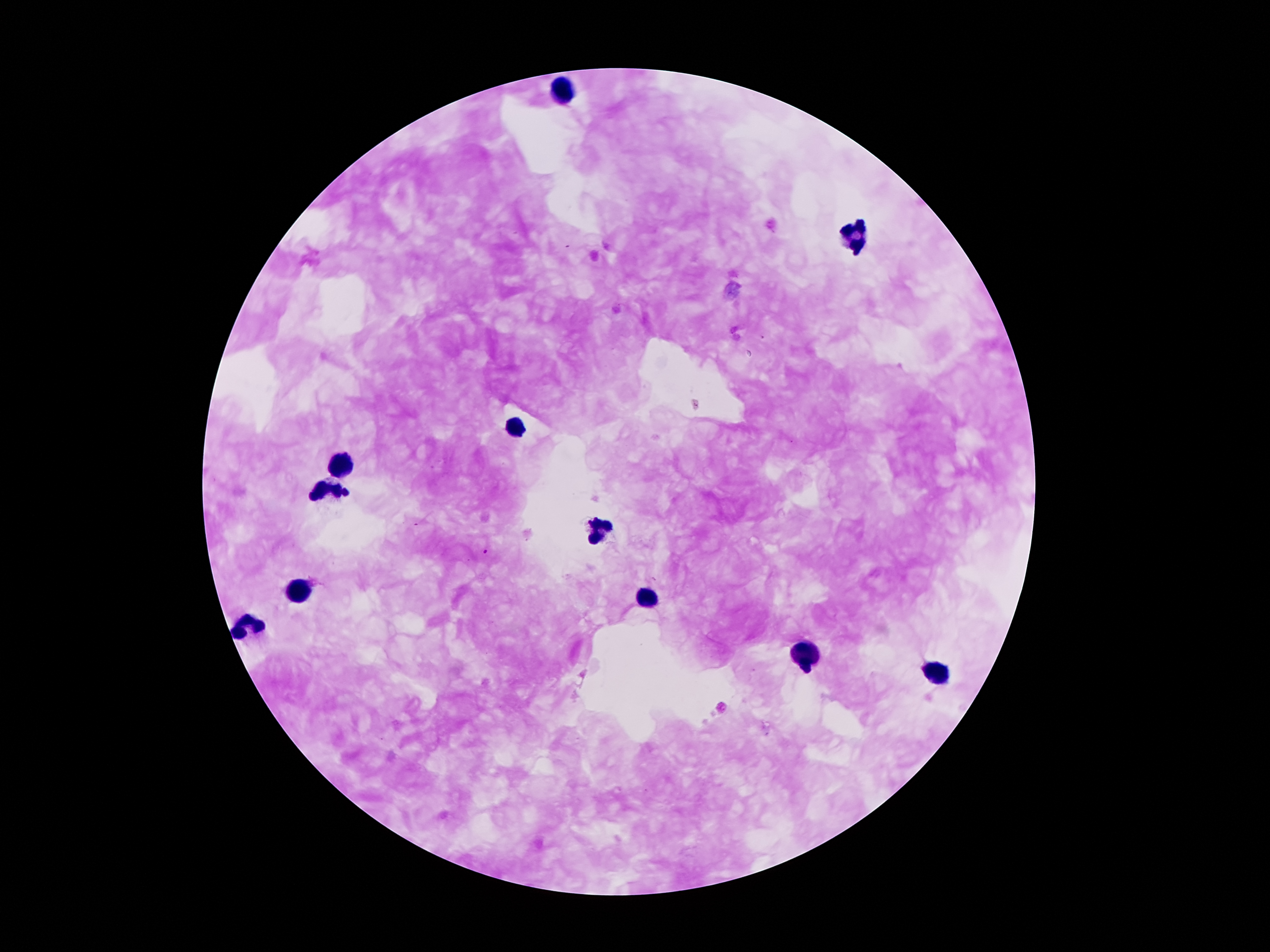
Approximate object centers, in pixels from the top-left corner. Leukocyte locations: (x=566, y=90), (x=855, y=235), (x=515, y=427), (x=343, y=464), (x=323, y=491), (x=595, y=537), (x=294, y=591), (x=648, y=600), (x=250, y=623), (x=806, y=659), (x=934, y=674). Malaria parasite locations: (x=484, y=552). 100x magnification. Patient malaria status: positive for Plasmodium falciparum. Smartphone photograph taken through the microscope eyepiece. One field from this slide. Thick blood smear. Giemsa-stained preparation. Image is 1270×952 pixels.